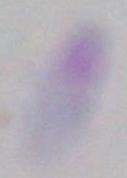
Summary:
  - Magnification: 1000x
  - Modality: photomicrograph
  - Identification: Toxoplasma gondii